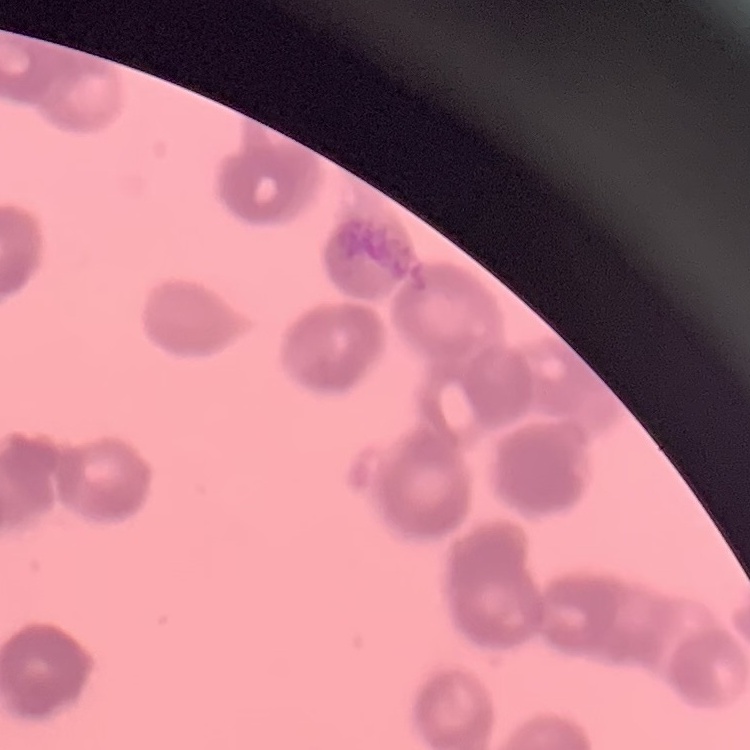

{
  "erythrocyte_morphology": "rouleaux formation",
  "preparation": "thin peripheral smear",
  "image_type": "square crop of a larger photomicrograph",
  "stain": "Field's or Giemsa"
}